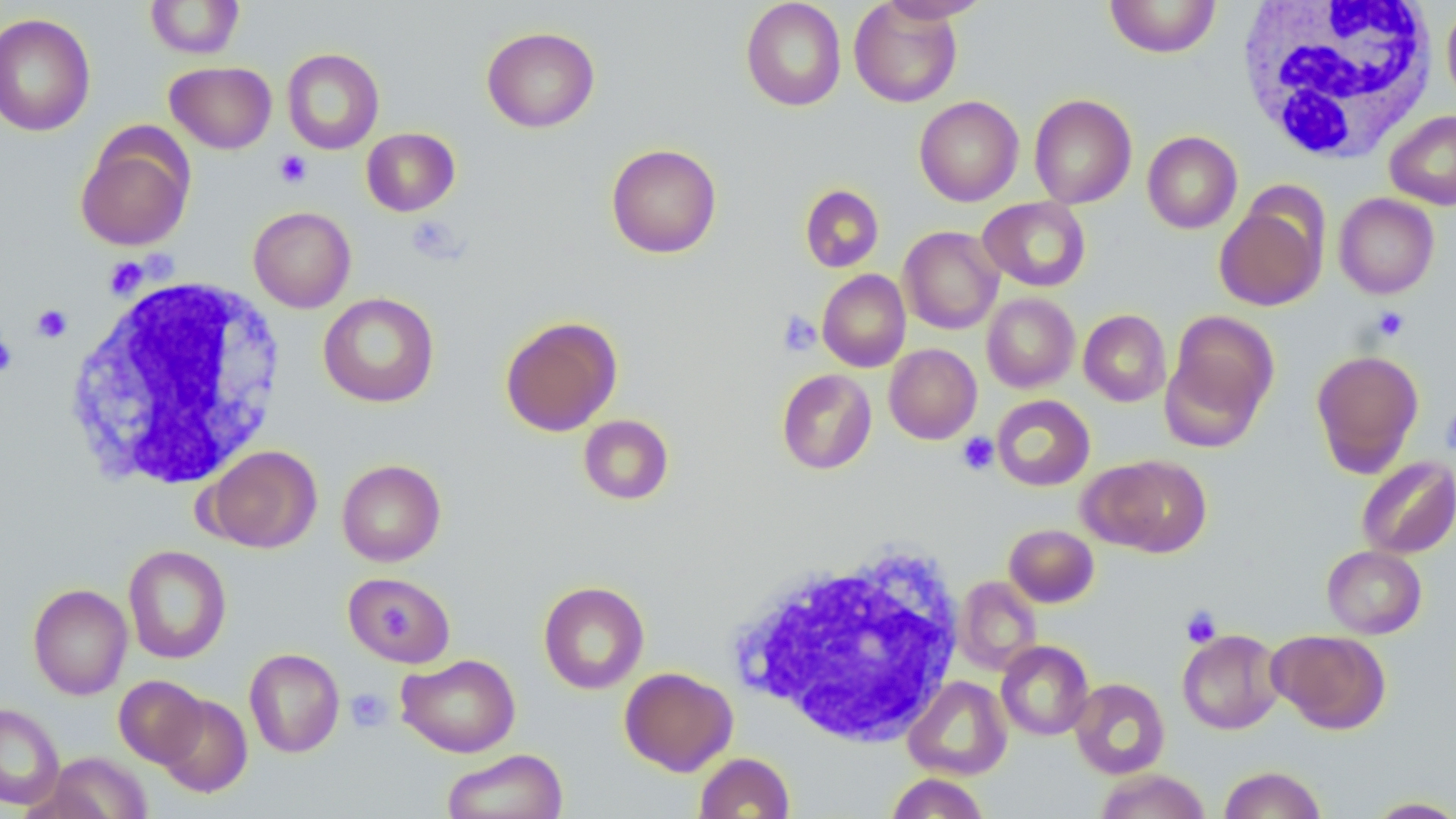 Approximate bounding boxes as named x1/y1/x2/y2 corners in pixels. Uninfected red blood cell locations: (x1=145, y1=0, x2=244, y2=59), (x1=741, y1=0, x2=847, y2=111), (x1=877, y1=0, x2=991, y2=23), (x1=1104, y1=0, x2=1221, y2=58), (x1=849, y1=1, x2=962, y2=108), (x1=1441, y1=5, x2=1456, y2=113), (x1=0, y1=13, x2=96, y2=137), (x1=481, y1=26, x2=600, y2=132), (x1=282, y1=48, x2=385, y2=154), (x1=166, y1=61, x2=277, y2=153), (x1=1029, y1=94, x2=1137, y2=209), (x1=914, y1=96, x2=1024, y2=206), (x1=1385, y1=110, x2=1456, y2=209), (x1=75, y1=126, x2=195, y2=252), (x1=361, y1=127, x2=460, y2=216), (x1=1142, y1=131, x2=1242, y2=234), (x1=606, y1=143, x2=722, y2=259), (x1=800, y1=184, x2=884, y2=272), (x1=1334, y1=193, x2=1439, y2=299), (x1=977, y1=197, x2=1091, y2=292), (x1=1214, y1=200, x2=1326, y2=310), (x1=248, y1=206, x2=356, y2=312), (x1=899, y1=226, x2=1004, y2=334), (x1=817, y1=269, x2=911, y2=372), (x1=318, y1=292, x2=439, y2=407), (x1=982, y1=293, x2=1079, y2=393), (x1=1078, y1=310, x2=1171, y2=407), (x1=1166, y1=310, x2=1279, y2=435), (x1=500, y1=316, x2=622, y2=436), (x1=884, y1=344, x2=982, y2=444), (x1=1311, y1=349, x2=1424, y2=477), (x1=776, y1=368, x2=877, y2=474), (x1=991, y1=395, x2=1095, y2=491), (x1=578, y1=414, x2=674, y2=505), (x1=203, y1=445, x2=322, y2=553), (x1=1086, y1=455, x2=1212, y2=557), (x1=1355, y1=455, x2=1456, y2=559), (x1=337, y1=459, x2=446, y2=566), (x1=1004, y1=523, x2=1099, y2=607), (x1=123, y1=544, x2=232, y2=664), (x1=1322, y1=545, x2=1427, y2=638), (x1=342, y1=571, x2=455, y2=667), (x1=954, y1=576, x2=1042, y2=675), (x1=538, y1=581, x2=649, y2=694), (x1=28, y1=583, x2=132, y2=700), (x1=1269, y1=629, x2=1391, y2=734), (x1=1177, y1=630, x2=1285, y2=734), (x1=996, y1=640, x2=1094, y2=740), (x1=244, y1=648, x2=345, y2=758), (x1=396, y1=653, x2=521, y2=757), (x1=619, y1=667, x2=738, y2=776), (x1=114, y1=675, x2=208, y2=767), (x1=903, y1=675, x2=1012, y2=780), (x1=1069, y1=678, x2=1170, y2=779), (x1=154, y1=694, x2=252, y2=797), (x1=0, y1=702, x2=64, y2=810), (x1=442, y1=749, x2=567, y2=819), (x1=43, y1=752, x2=151, y2=818), (x1=693, y1=752, x2=795, y2=818), (x1=1218, y1=765, x2=1327, y2=818), (x1=1093, y1=768, x2=1211, y2=819), (x1=885, y1=772, x2=990, y2=818), (x1=1363, y1=796, x2=1456, y2=818). Platelet locations: (x1=274, y1=150, x2=312, y2=189), (x1=406, y1=215, x2=464, y2=264), (x1=104, y1=257, x2=148, y2=298), (x1=32, y1=304, x2=73, y2=343), (x1=1372, y1=306, x2=1409, y2=342), (x1=777, y1=311, x2=822, y2=356), (x1=0, y1=333, x2=18, y2=377), (x1=1441, y1=406, x2=1456, y2=457), (x1=957, y1=432, x2=999, y2=475), (x1=1181, y1=605, x2=1221, y2=648), (x1=345, y1=687, x2=393, y2=733). White blood cell locations: (x1=1235, y1=0, x2=1438, y2=164), (x1=62, y1=273, x2=288, y2=491), (x1=732, y1=540, x2=967, y2=746). Slide-level diagnosis: no evidence of blood parasites. Captured at 1000x magnification. Image is 1456×819 pixels. Light microscopy. Single field of view. May-Grünwald-Giemsa stain. Thin blood smear.